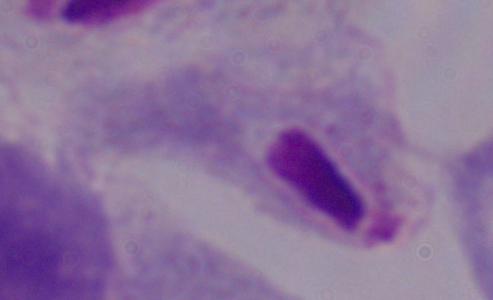

Summary:
  - Modality: micrograph
  - Magnification: 1000x
  - Identification: trichomonad